Assess for malaria.
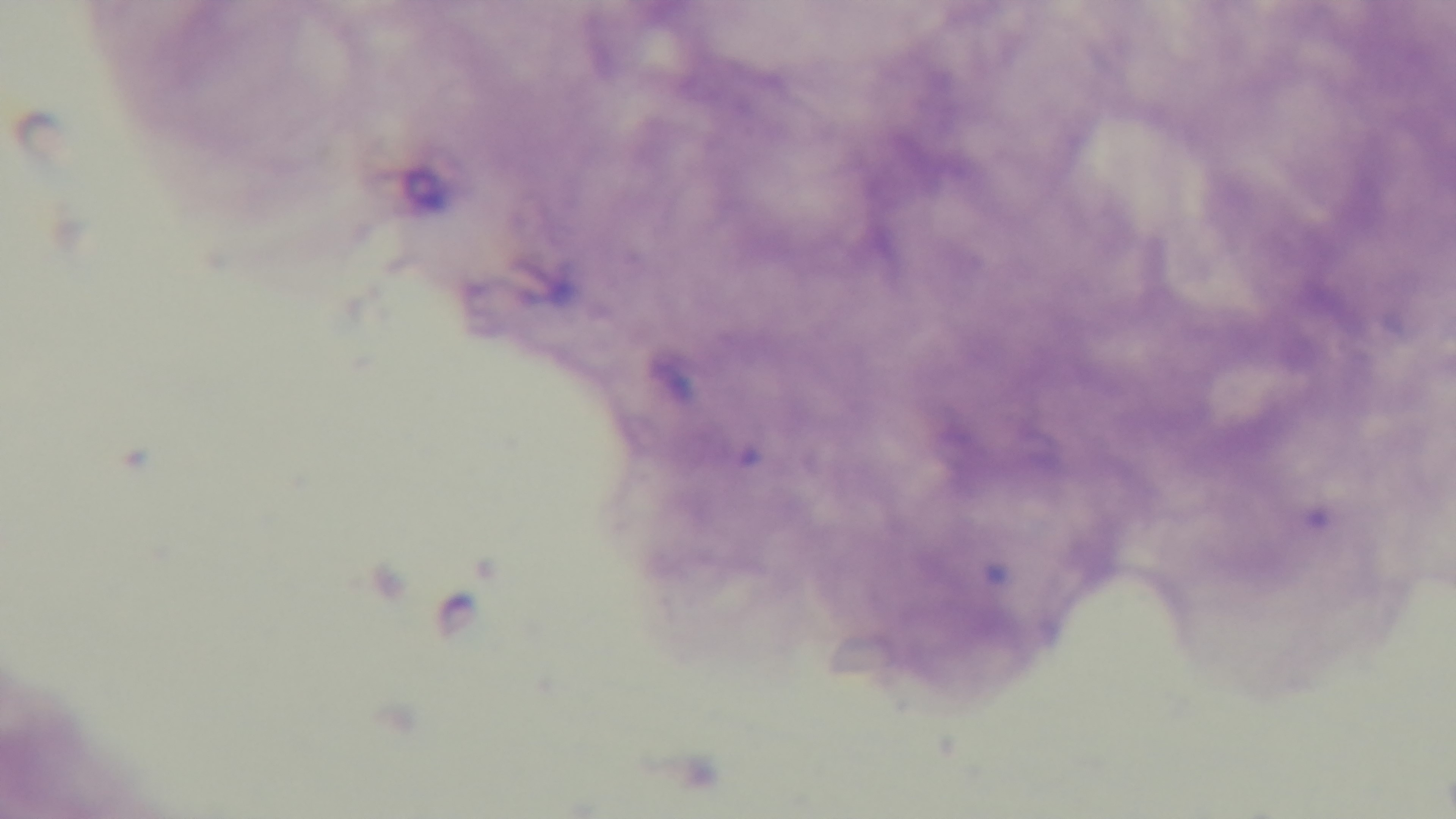

It is uninfected.

{
  "objective": "100x oil immersion",
  "preparation": "thick blood film",
  "capture": "mounted 4K digital camera",
  "modality": "light microscopy",
  "stain": "Giemsa",
  "field_of_view": "single"
}